State which parasite is depicted.
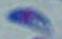

Toxoplasma gondii.

Summary:
  - Magnification: 1000x
  - Modality: photomicrograph